Locate every leukocyte (white blood cell).
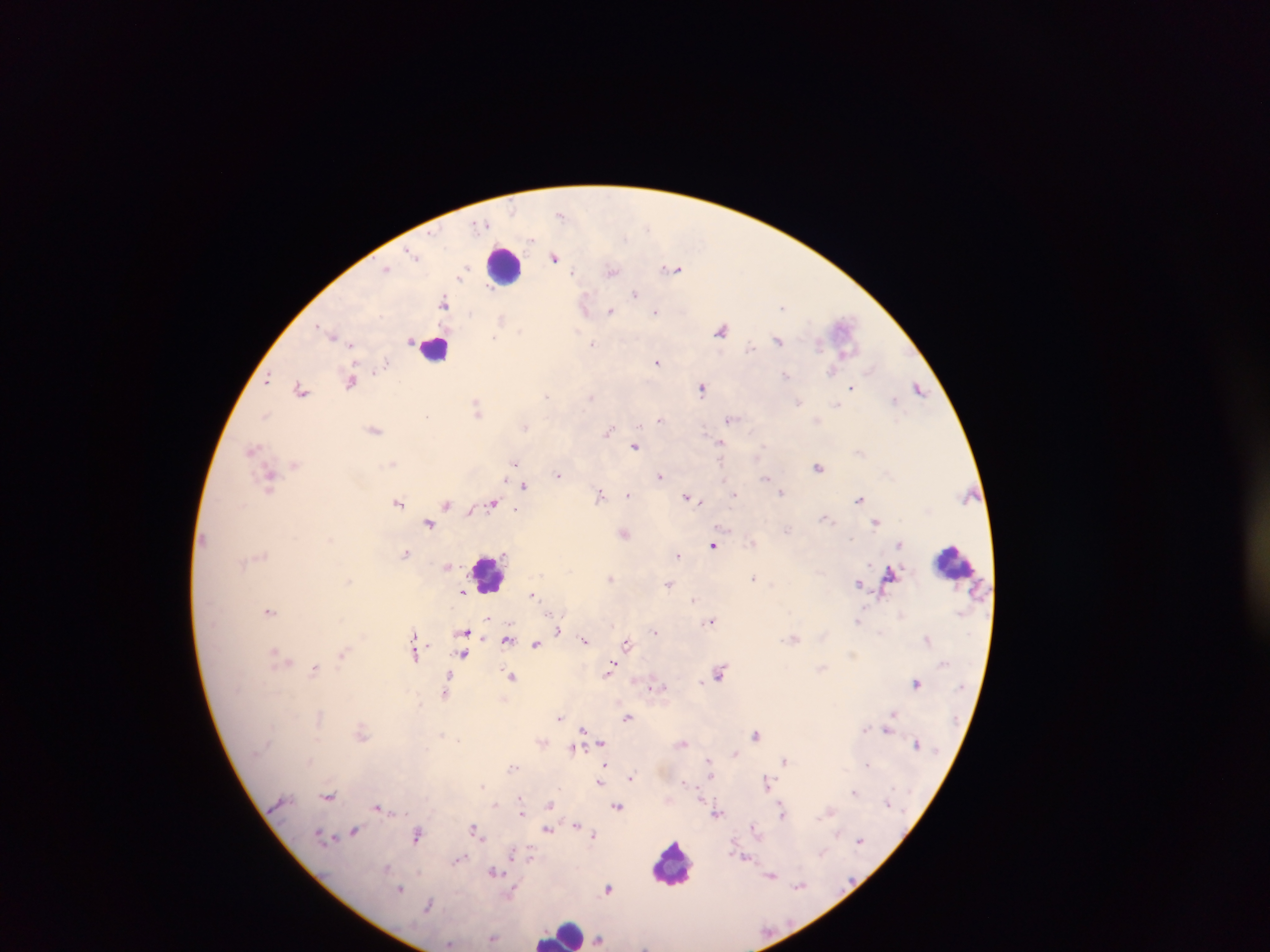

Approximate centers as {x, y} in pixels.
Leukocytes: {505, 266}, {434, 347}, {954, 562}, {488, 574}, {672, 862}, {562, 932}.

image_size: 1270×952 pixels
capture: mobile-phone photograph through a microscope
malaria_parasite_locations: 'approximate centers as {x, y} in pixels: {560, 214}, {482, 224}, {531, 239}, {413, 254}, {555, 258}, {387, 268}, {674, 269}, {572, 271}, {612, 272}, {460, 276}, {487, 287}, {634, 293}, {445, 302}, {585, 304}, {782, 307}, {611, 311}, {656, 311}, {501, 318}, {318, 326}, {721, 330}, {331, 334}, {339, 338}, {494, 338}, {778, 340}, {411, 341}, {593, 344}, {351, 345}, {751, 348}, {658, 362}, {386, 363}, {832, 371}, {785, 375}, {268, 379}, {351, 382}, {851, 388}, {301, 389}, {702, 389}, {919, 389}, {547, 395}, {591, 397}, {894, 400}, {798, 402}, {837, 405}, {476, 407}, {265, 415}, {427, 416}, {731, 418}, {660, 420}, {525, 427}, {376, 430}, {609, 430}, {720, 442}, {635, 446}, {252, 448}, {513, 462}, {392, 464}, {295, 465}, {818, 466}, {558, 475}, {660, 476}, {766, 477}, {269, 479}, {506, 479}, {524, 485}, {781, 492}, {600, 494}, {627, 494}, {735, 494}, {690, 497}, {859, 499}, {695, 500}, {398, 503}, {446, 504}, {492, 504}, {471, 510}, {516, 510}, {825, 519}, {876, 521}, {430, 523}, {787, 529}, {625, 533}, {753, 543}, {900, 544}, {713, 545}, {405, 554}, {677, 556}, {449, 566}, {611, 578}, {754, 578}, {348, 581}, {669, 583}, {858, 583}, {463, 592}, {533, 595}, {694, 599}, {269, 611}, {488, 618}, {711, 620}, {858, 620}, {559, 630}, {654, 631}, {464, 633}, {881, 633}, {415, 635}, {794, 638}, {507, 639}, {927, 639}, {585, 640}, {627, 644}, {535, 645}, {416, 652}, {275, 653}, {343, 654}, {464, 654}, {282, 660}, {315, 669}, {609, 670}, {720, 672}, {512, 677}, {446, 682}, {916, 683}, {657, 686}, {444, 691}, {892, 713}, {558, 717}, {627, 718}, {584, 730}, {886, 730}, {361, 733}, {442, 734}, {756, 734}, {458, 739}, {602, 742}, {684, 743}, {917, 744}, {573, 749}, {736, 753}, {709, 760}, {785, 760}, {605, 765}, {867, 765}, {513, 768}, {711, 775}, {631, 778}, {684, 782}, {600, 783}, {767, 783}, {483, 786}, {854, 792}, {330, 796}, {522, 803}, {887, 803}, {496, 804}, {550, 804}, {617, 806}, {379, 808}, {781, 808}, {521, 811}, {829, 812}, {718, 813}, {577, 825}, {753, 827}, {475, 829}, {547, 830}, {355, 831}, {418, 834}, {594, 835}, {323, 837}, {860, 839}, {514, 854}, {530, 858}, {460, 859}, {387, 868}, {494, 872}, {772, 876}, {799, 886}, {608, 888}, {401, 889}, {514, 892}, {429, 905}, {493, 939}, {600, 939}, {450, 943}'
preparation: thick blood smear
country: Ghana
field_of_view: single